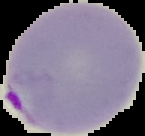
image size = 145×136 pixels
malaria status = parasitized
image type = segmented cell region on a black background
preparation = thin blood film